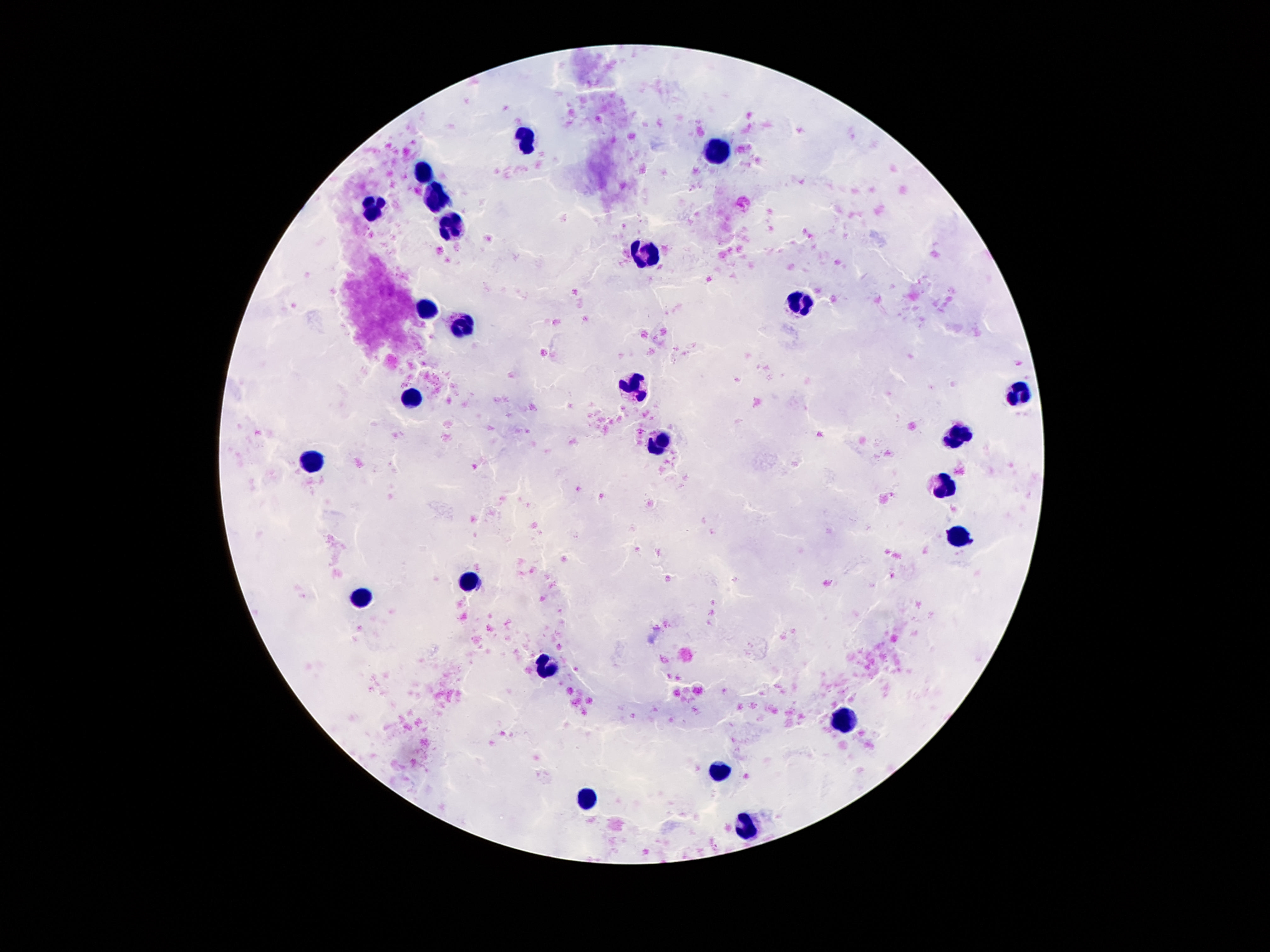

Approximate centers as [x, y] in pixels.
Summary:
  - Leukocyte locations: [526, 137], [714, 153], [423, 172], [434, 196], [372, 203], [452, 231], [646, 253], [800, 303], [421, 309], [460, 324], [636, 385], [1019, 391], [415, 400], [960, 436], [661, 445], [313, 462], [941, 486], [954, 538], [472, 582], [360, 596], [546, 667], [843, 723], [718, 772], [585, 797], [745, 828]
  - Field of view: single
  - Image size: 1270×952 pixels
  - Patient malaria status: uninfected
  - Preparation: thick blood film
  - Magnification: 100x
  - Stain: Giemsa
  - Capture: smartphone camera through the microscope eyepiece